Assess this cell for malaria.
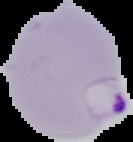

Parasitized.

Image is 133×142 pixels. Cell region segmented out of the field of view; the surrounding area is masked to black. From a thin blood smear.